Point out each Plasmodium parasite.
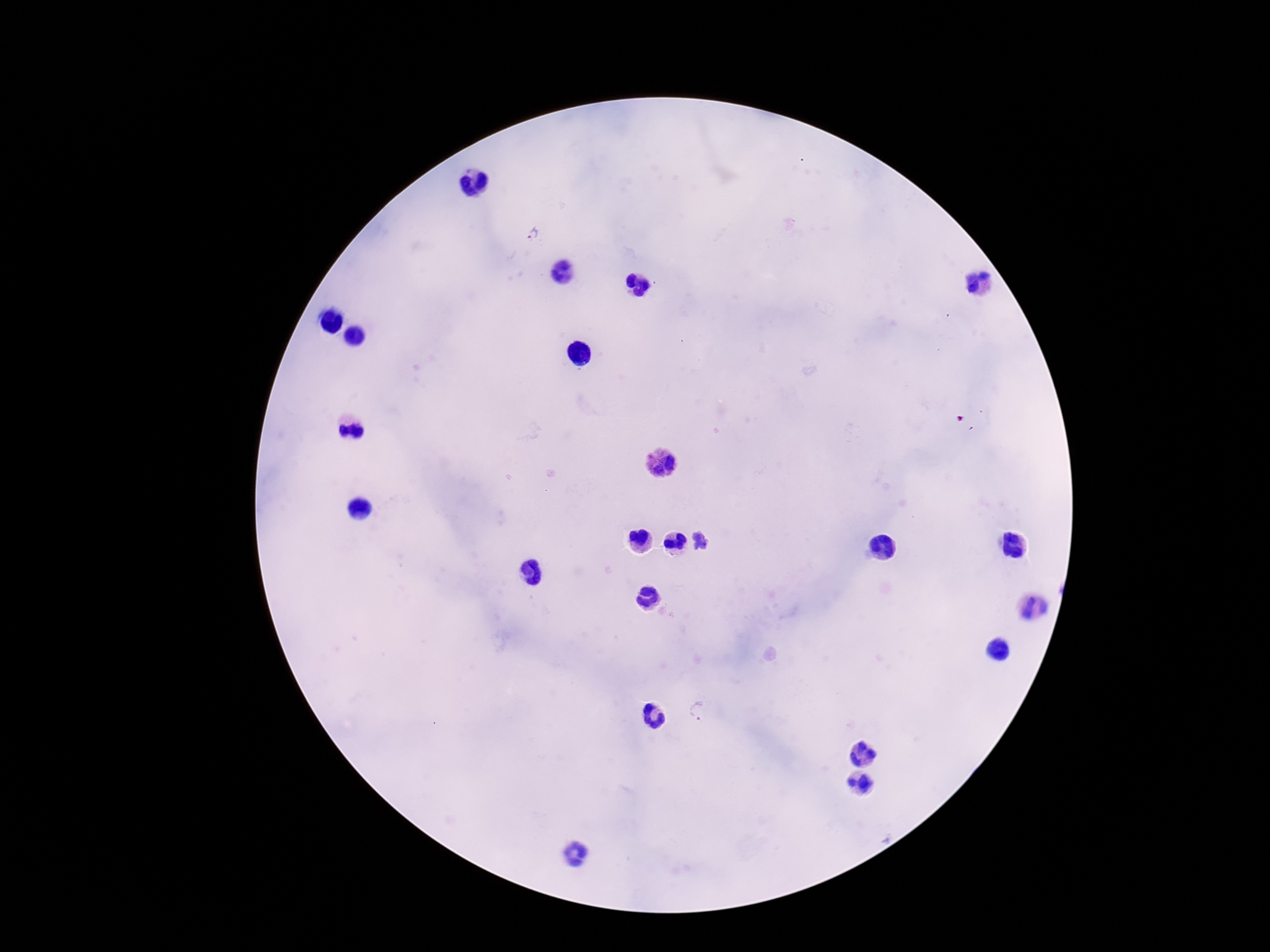

Approximate centers as (x, y) in pixels.
Plasmodium parasites: (531, 234), (700, 710).

Patient malaria status: positive. 100x magnification. Thick blood smear. Image is 1270×952 pixels. Photographed through the microscope eyepiece with a smartphone camera. Single field of view. Giemsa stain.